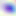
Summary:
  - Modality: photomicrograph
  - Identification: Toxoplasma gondii
  - Magnification: 400x